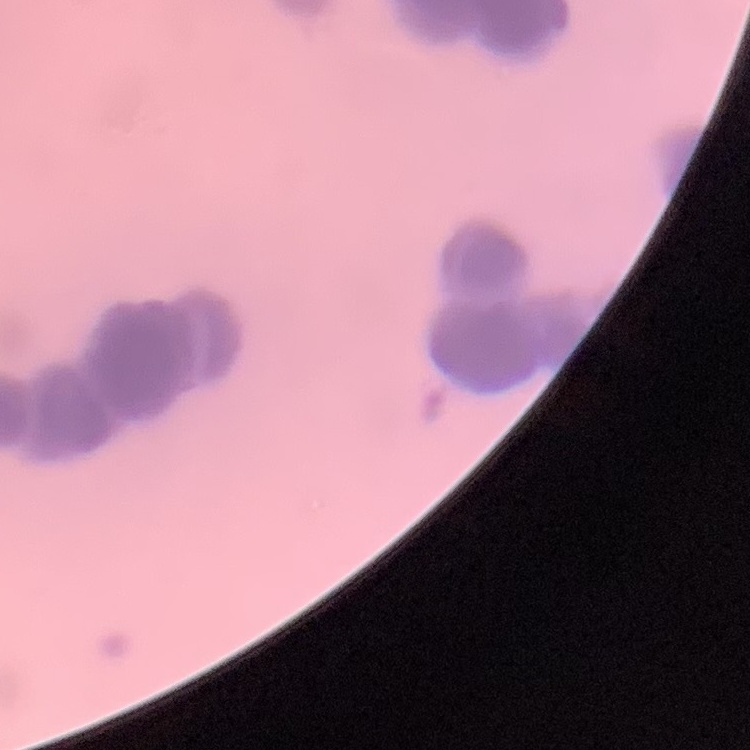
The red blood cells exhibit rouleaux formation. Stained with either Field's or Giemsa. Thin peripheral smear. One tile cut from a larger photomicrograph.